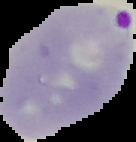
result: malaria parasites detected
image_type: segmented cell region on a black background
image_size: 136×142 pixels
preparation: thin blood film